Report the malaria status of this cell.
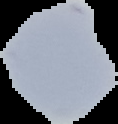

Uninfected.

Segmented cell region on a black background. From a thin blood film. Image is 118×124 pixels.